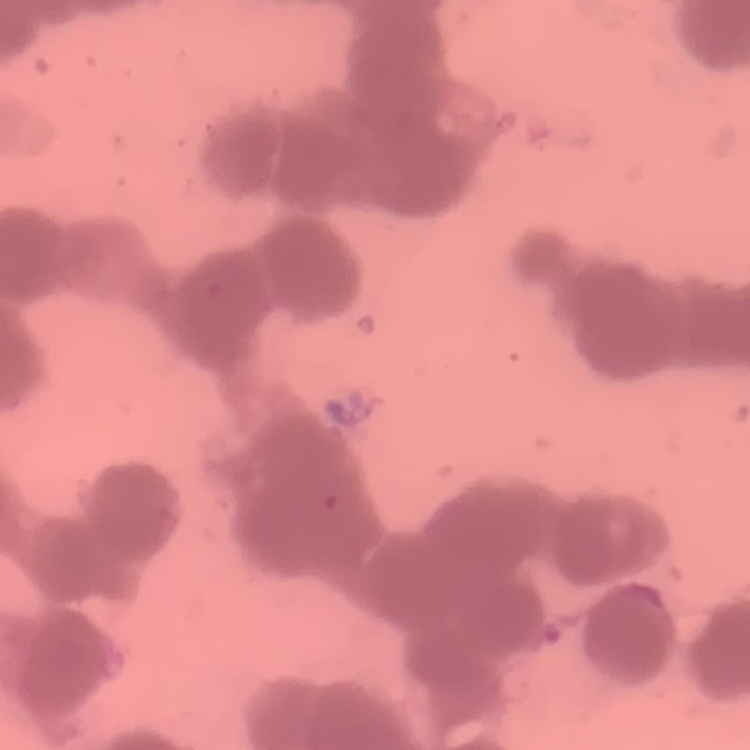

{
  "red_blood_cell_morphology": "rouleaux formation",
  "preparation": "thin blood smear",
  "image_type": "one tile cut from a larger photomicrograph",
  "stain": "Field's or Giemsa"
}